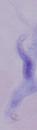

Summary:
  - Magnification: 1000x
  - Modality: micrograph
  - Identification: trypanosome